Assess for parasitized red blood cells.
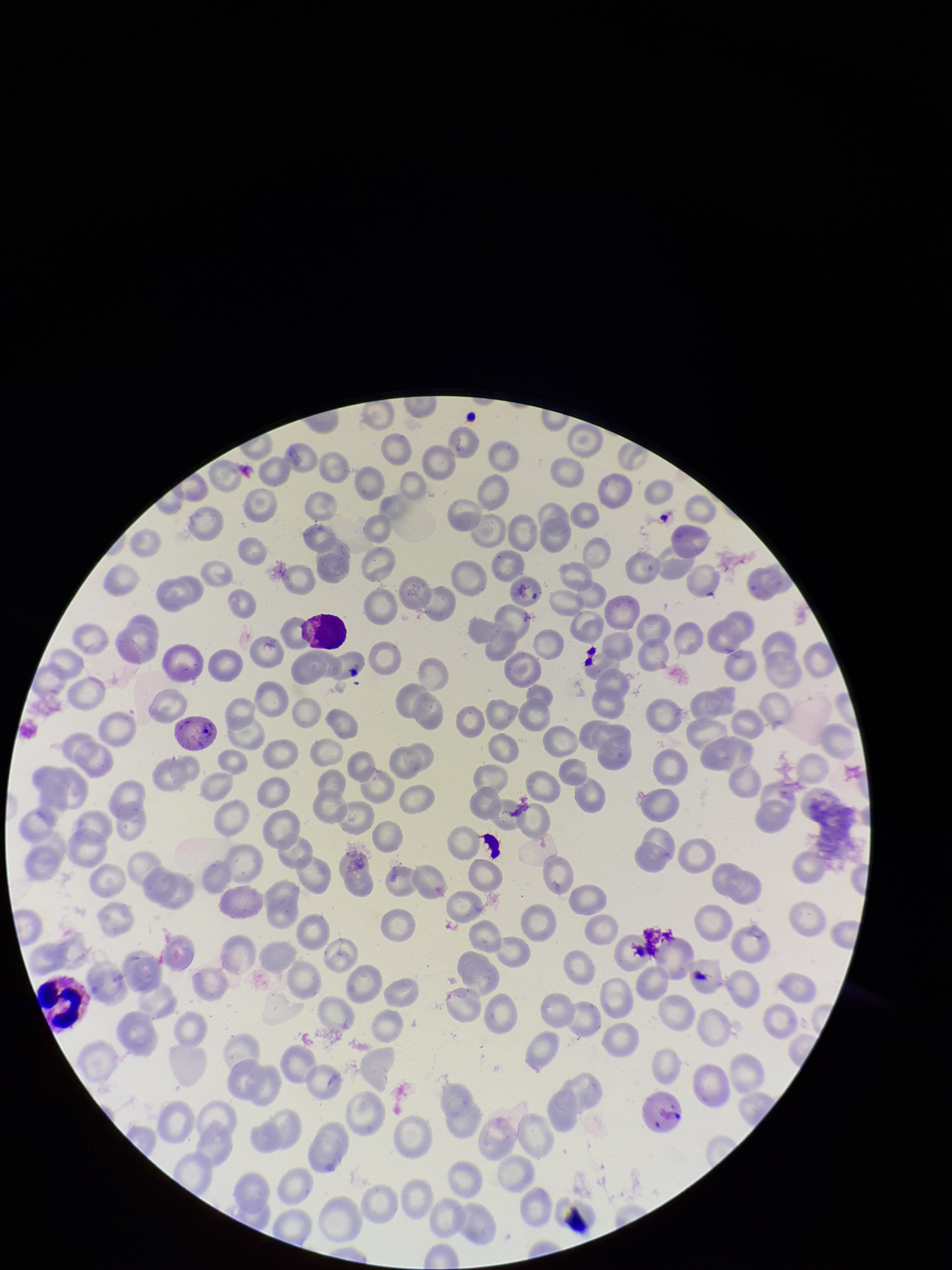
Identified.

Summary:
  - Parasitized red blood cell count: 1
  - Red blood cell count: 200
  - Stain: Giemsa
  - Species reported for this patient: Plasmodium vivax
  - Capture: smartphone photograph through the microscope eyepiece
  - Field of view: one from this slide
  - Patient malaria status: infected
  - Image size: 952×1270 pixels
  - Preparation: thin blood smear